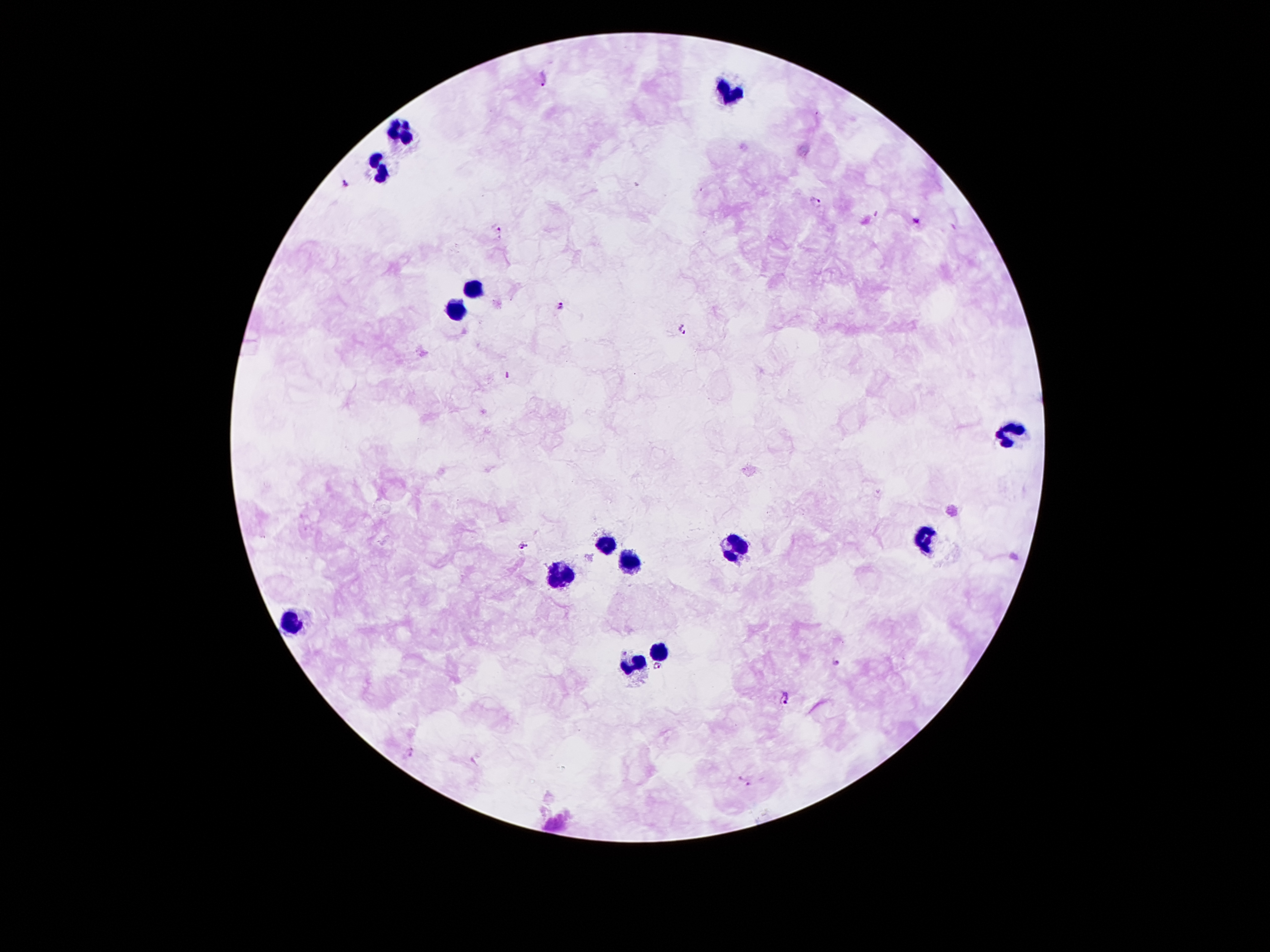

Approximate object centers, in pixels from the top-left corner. Leukocyte locations: (x=728, y=89), (x=400, y=126), (x=378, y=168), (x=473, y=288), (x=456, y=310), (x=1015, y=432), (x=923, y=538), (x=603, y=546), (x=738, y=548), (x=630, y=564), (x=562, y=575), (x=291, y=619), (x=660, y=649), (x=635, y=662). Malaria parasite locations: (x=544, y=80), (x=346, y=183), (x=819, y=202), (x=916, y=221), (x=497, y=227), (x=561, y=307), (x=681, y=330), (x=507, y=375), (x=522, y=546), (x=836, y=662), (x=658, y=667), (x=786, y=699), (x=745, y=782). Patient malaria status: positive for Plasmodium falciparum. Thick peripheral-blood smear. Image is 1270×952 pixels. One field from this slide. Smartphone photograph taken through the microscope eyepiece. Giemsa stain. 100x magnification.